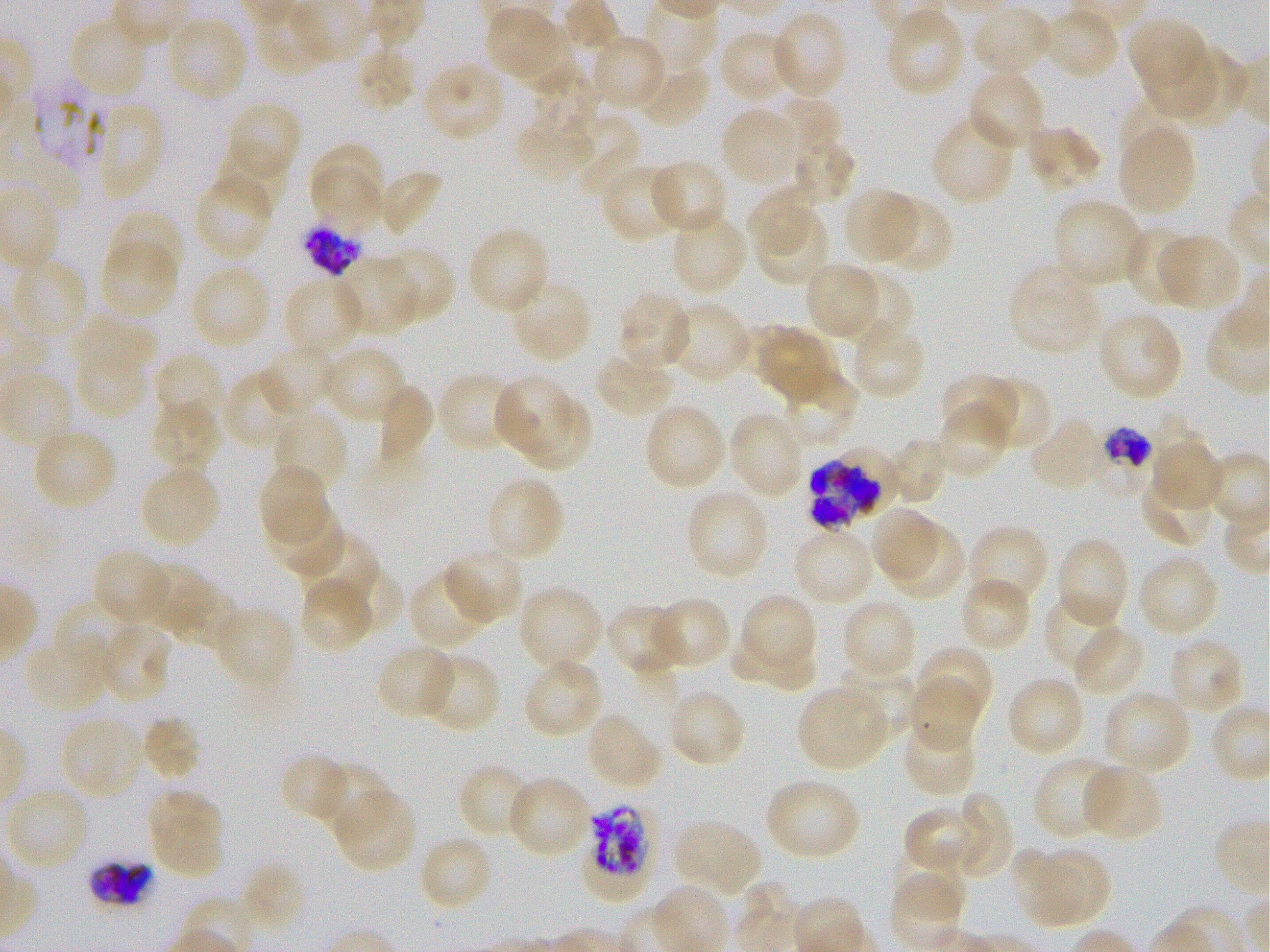

Not every red blood cell is marked. A life-cycle stage — or a range of stages, where the recorded stages span more than one — follows each staged infected red blood cell.
culture = static in-vitro Plasmodium falciparum strain 3D7
preparation = thin blood smear
locations of infected red blood cells = approximate bounding boxes as [x1, y1, x2, y2] in pixels: [300, 222, 364, 276]; [1089, 428, 1153, 498] trophozoite; [811, 463, 879, 534]; [584, 801, 659, 901] late trophozoite to late schizont; [86, 858, 155, 908]
donor blood group = O+
field of view = single
objective = 100x, oil immersion, numerical aperture 1.25
locations of uninfected red blood cells = approximate bounding boxes as [x1, y1, x2, y2] in pixels: [972, 4, 1054, 78], [1044, 7, 1119, 81], [485, 8, 563, 82], [884, 8, 966, 97], [770, 10, 849, 99], [68, 15, 148, 98], [166, 15, 249, 103], [1127, 17, 1209, 96], [719, 30, 797, 105], [591, 35, 667, 110], [1140, 41, 1219, 120], [353, 46, 417, 112], [1174, 47, 1252, 128], [421, 62, 506, 143], [635, 62, 712, 128], [968, 70, 1046, 152], [533, 72, 597, 142], [1123, 94, 1194, 160], [774, 97, 843, 161], [223, 100, 303, 180], [95, 101, 165, 201], [720, 107, 800, 186], [515, 113, 594, 184], [566, 113, 640, 198], [931, 113, 1017, 205], [1024, 125, 1104, 194], [1119, 127, 1197, 215], [791, 136, 856, 205], [310, 144, 384, 209], [216, 146, 289, 217], [650, 159, 729, 236], [601, 162, 685, 243], [313, 165, 385, 235], [377, 169, 444, 237], [194, 173, 274, 260], [748, 186, 818, 260], [843, 188, 918, 264], [879, 196, 954, 274], [1052, 199, 1144, 288], [106, 209, 184, 280], [756, 210, 830, 289], [670, 211, 747, 295], [1122, 224, 1198, 307], [467, 226, 550, 315], [1157, 234, 1242, 311], [100, 239, 178, 319], [379, 247, 456, 324], [336, 256, 418, 335], [11, 259, 89, 341], [805, 262, 882, 338], [189, 263, 272, 350], [1008, 264, 1100, 355], [845, 269, 916, 345], [283, 275, 365, 358], [507, 279, 593, 364], [617, 291, 692, 372], [846, 299, 922, 375], [666, 300, 751, 384], [1098, 311, 1185, 400], [71, 313, 157, 376], [849, 321, 927, 400], [757, 326, 829, 399], [259, 343, 335, 415], [322, 344, 408, 424], [75, 346, 145, 419], [593, 351, 676, 419], [154, 353, 226, 430], [781, 369, 859, 446], [222, 370, 298, 451], [436, 371, 520, 452], [937, 371, 1018, 443], [975, 375, 1050, 452], [499, 379, 571, 455], [373, 384, 435, 464], [522, 399, 589, 471], [149, 400, 221, 474], [935, 401, 1013, 479], [642, 402, 727, 491], [271, 409, 349, 494], [728, 412, 804, 500], [1147, 414, 1209, 476], [1028, 416, 1106, 493], [31, 427, 118, 510], [886, 437, 950, 505], [1153, 443, 1226, 511], [257, 464, 329, 544], [139, 465, 221, 548], [1139, 475, 1214, 547], [487, 481, 563, 558], [684, 488, 771, 580], [265, 501, 344, 577], [869, 509, 943, 581], [888, 524, 966, 600], [967, 524, 1050, 608], [792, 525, 874, 606], [296, 531, 380, 615], [1056, 536, 1130, 627], [92, 549, 172, 625], [444, 549, 525, 624], [1137, 553, 1221, 638], [141, 561, 210, 634], [408, 568, 491, 651], [341, 569, 402, 631], [298, 577, 372, 653], [960, 577, 1032, 653], [176, 582, 241, 654], [517, 584, 603, 672], [738, 593, 817, 673], [1044, 594, 1122, 673], [651, 595, 732, 670], [51, 597, 137, 675], [841, 599, 918, 680], [604, 603, 683, 677], [212, 605, 297, 690], [98, 622, 172, 705], [1071, 624, 1146, 698], [1167, 637, 1245, 716], [24, 638, 110, 714], [375, 643, 458, 719], [733, 643, 816, 690], [917, 644, 994, 720], [421, 653, 501, 734], [523, 659, 604, 738], [839, 666, 918, 741], [908, 675, 981, 750], [1006, 676, 1085, 758], [797, 684, 888, 771], [666, 688, 748, 768], [1101, 690, 1193, 775], [586, 712, 663, 791], [140, 714, 203, 781], [59, 716, 143, 800], [901, 719, 977, 796], [282, 755, 346, 819], [1032, 755, 1125, 841], [317, 763, 391, 837], [1080, 763, 1163, 840], [461, 766, 533, 835], [512, 778, 586, 853], [764, 778, 861, 860], [5, 786, 90, 872], [146, 789, 223, 851], [332, 789, 415, 873], [953, 791, 1015, 881], [903, 805, 979, 875], [151, 817, 224, 878], [674, 819, 763, 898], [424, 838, 488, 905], [1012, 847, 1082, 928], [894, 849, 969, 920], [1037, 850, 1109, 926], [239, 861, 308, 933], [889, 876, 961, 948]
stain = Giemsa
locations of red blood cells of indeterminate infection status = approximate bounding boxes as [x1, y1, x2, y2] in pixels: [32, 76, 109, 170], [836, 447, 901, 518]
image size = 1270×952 pixels